Assess for malaria.
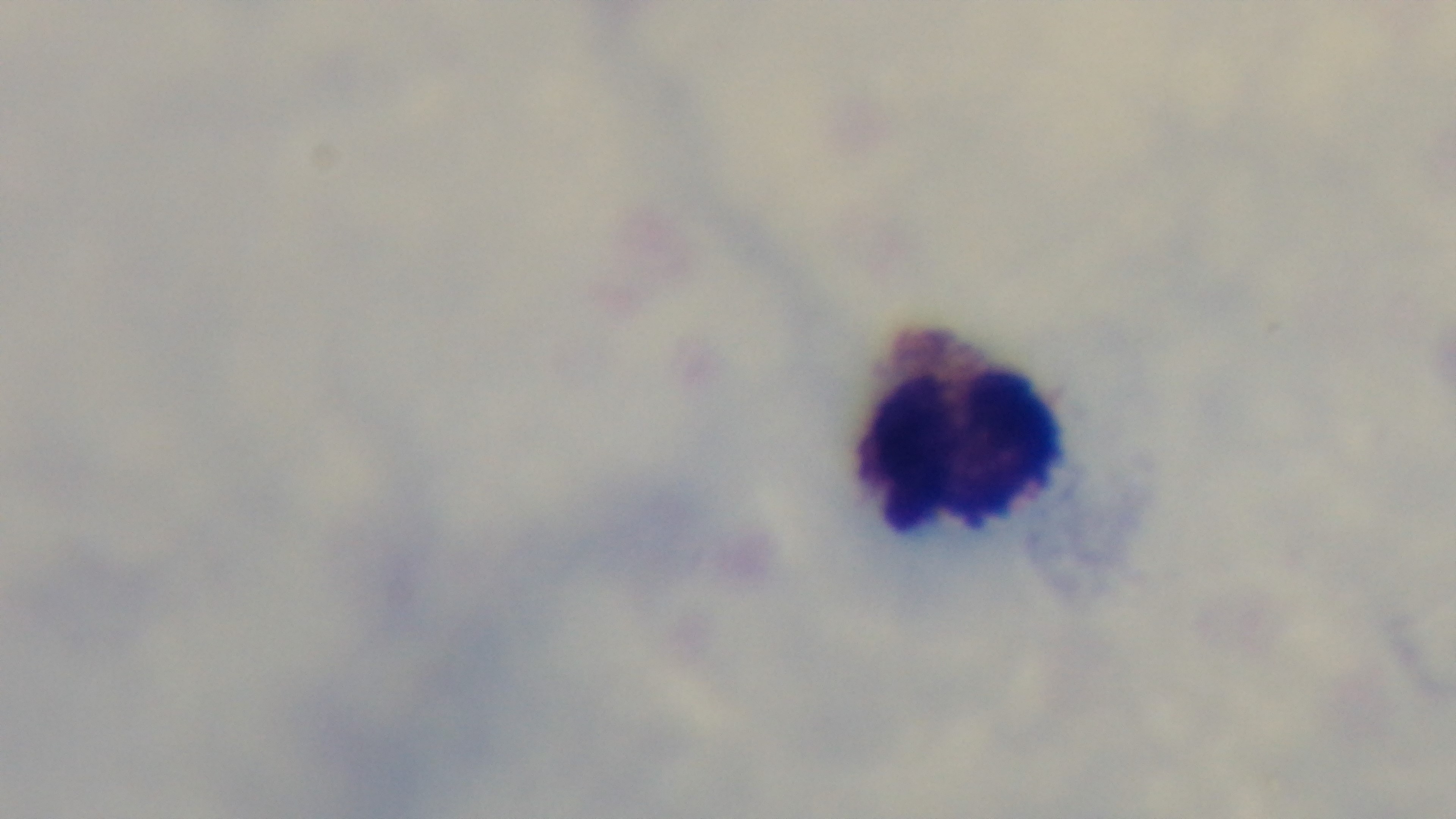

Uninfected.

Single field of view. Giemsa-stained. Light microscopy. Mounted 4K digital camera. Preparation: thick blood film. 100x oil-immersion objective.